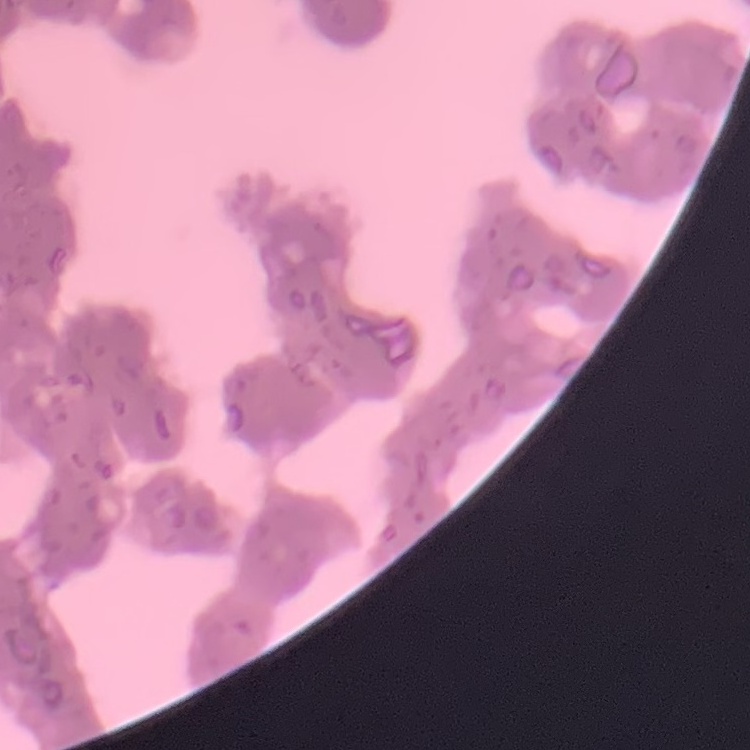 The red blood cells exhibit rouleaux formation. Field's or Giemsa stain. Thin blood smear. Square crop of a larger photomicrograph.